Locate every white blood cell.
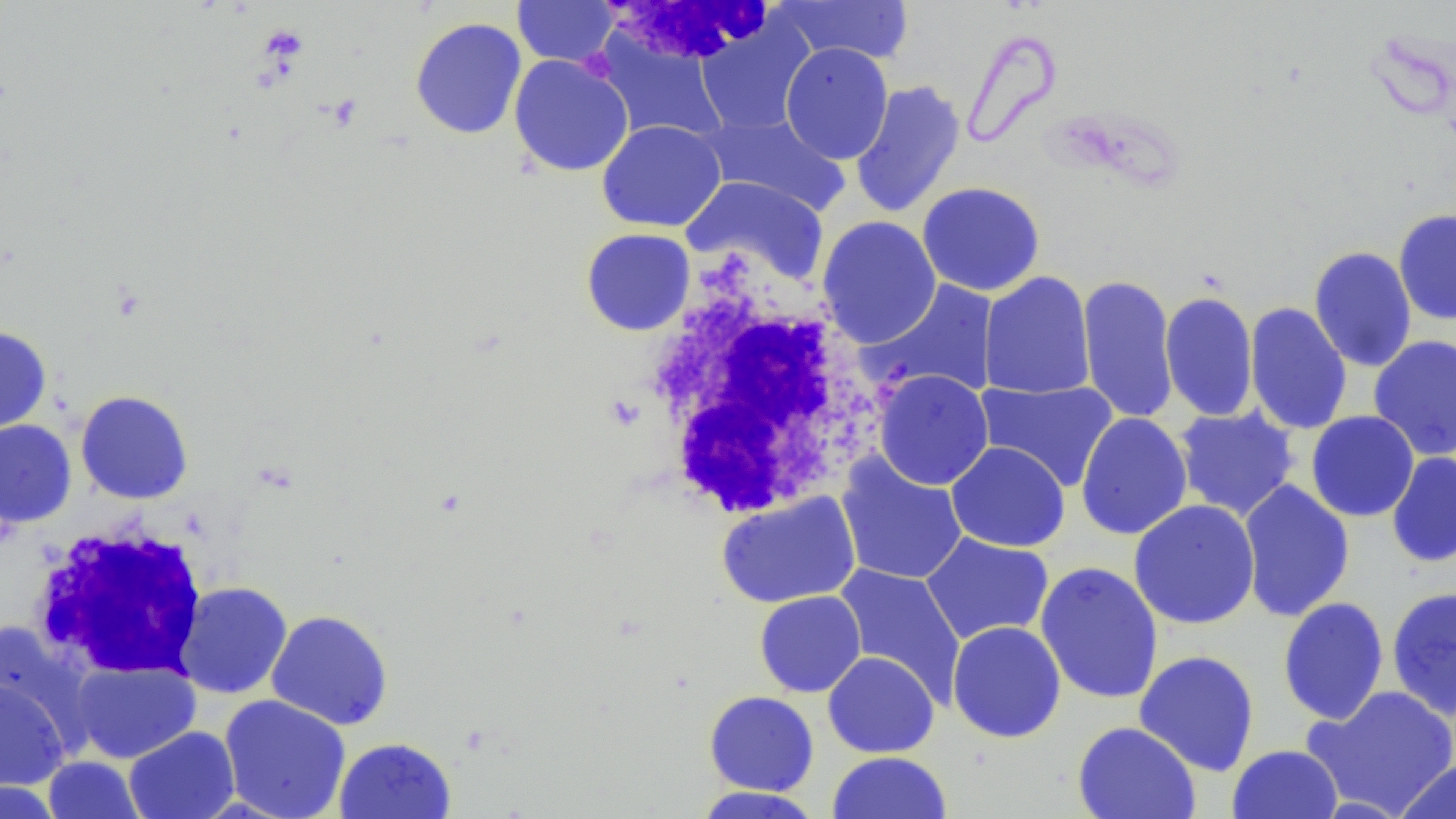
Approximate bounding boxes as (x1, y1, x2, y2) in pixels.
White blood cells: (606, 3, 783, 64), (638, 259, 886, 518), (28, 522, 211, 682).

slide_level_diagnosis: no evidence of blood parasites
field_of_view: one of a larger specimen
modality: light microscopy
stain: May-Grünwald-Giemsa
preparation: thin blood film
image_size: 1456×819 pixels
uninfected_red_blood_cell_locations: 'approximate bounding boxes as (x1, y1, x2, y2) in pixels: (772, 0, 915, 65), (512, 1, 619, 68), (410, 17, 527, 140), (696, 21, 815, 135), (596, 33, 728, 144), (780, 42, 893, 164), (509, 54, 634, 177), (849, 79, 966, 219), (700, 112, 850, 216), (596, 120, 726, 232), (681, 175, 830, 286), (916, 181, 1045, 297), (1393, 209, 1456, 325), (816, 216, 942, 348), (580, 228, 696, 335), (1309, 246, 1417, 372), (979, 271, 1095, 400), (1077, 274, 1179, 425), (867, 280, 1000, 401), (1160, 291, 1259, 422), (1244, 302, 1352, 435), (0, 326, 52, 435), (1368, 334, 1456, 461), (873, 370, 994, 490), (976, 379, 1118, 493), (75, 390, 194, 504), (1174, 406, 1299, 521), (1306, 411, 1419, 522), (1075, 412, 1193, 540), (0, 419, 77, 527), (946, 441, 1070, 552), (1386, 452, 1456, 568), (836, 453, 968, 585), (1238, 480, 1355, 622), (716, 492, 860, 609), (1128, 499, 1261, 629), (920, 532, 1054, 645), (1035, 561, 1164, 705), (833, 564, 966, 703), (174, 581, 292, 699), (1386, 586, 1456, 721), (754, 591, 866, 697), (1277, 597, 1390, 725), (266, 609, 394, 730), (946, 620, 1067, 743), (1, 621, 93, 747), (1133, 649, 1260, 777), (822, 651, 939, 758), (70, 659, 200, 764), (0, 677, 69, 791), (1302, 685, 1456, 817), (704, 690, 819, 796), (219, 694, 351, 819), (1072, 721, 1201, 819), (123, 726, 240, 819), (334, 737, 456, 819), (1227, 744, 1343, 819), (827, 751, 952, 819), (42, 755, 146, 818), (1393, 758, 1456, 819), (0, 780, 64, 818), (691, 786, 826, 818)'
platelet_locations: 'approximate bounding boxes as (x1, y1, x2, y2) in pixels: (260, 26, 309, 62)'
magnification: 1000x